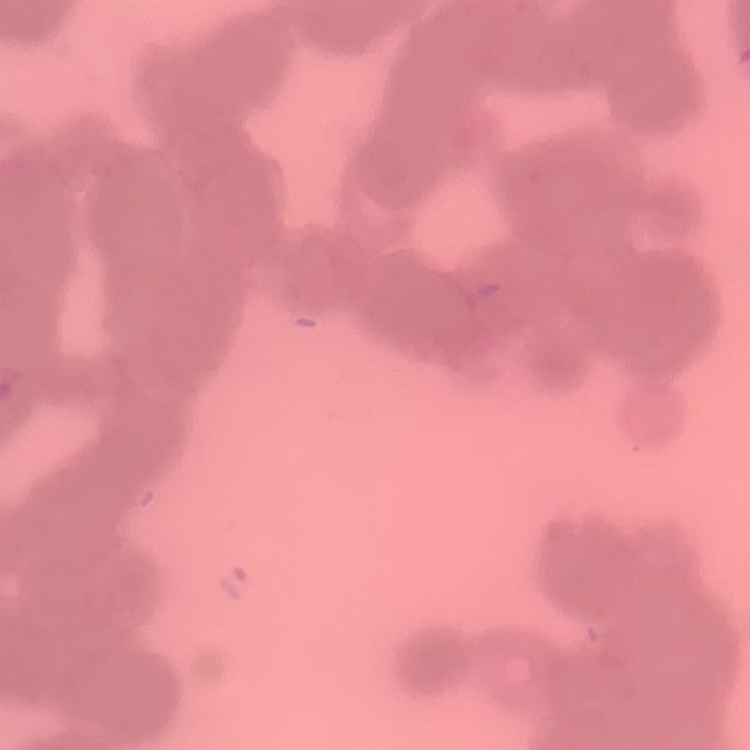

The red blood cells show rouleaux formation. Thin blood film. One tile cut from a larger photomicrograph. Field's or Giemsa stain.